Assess for malaria.
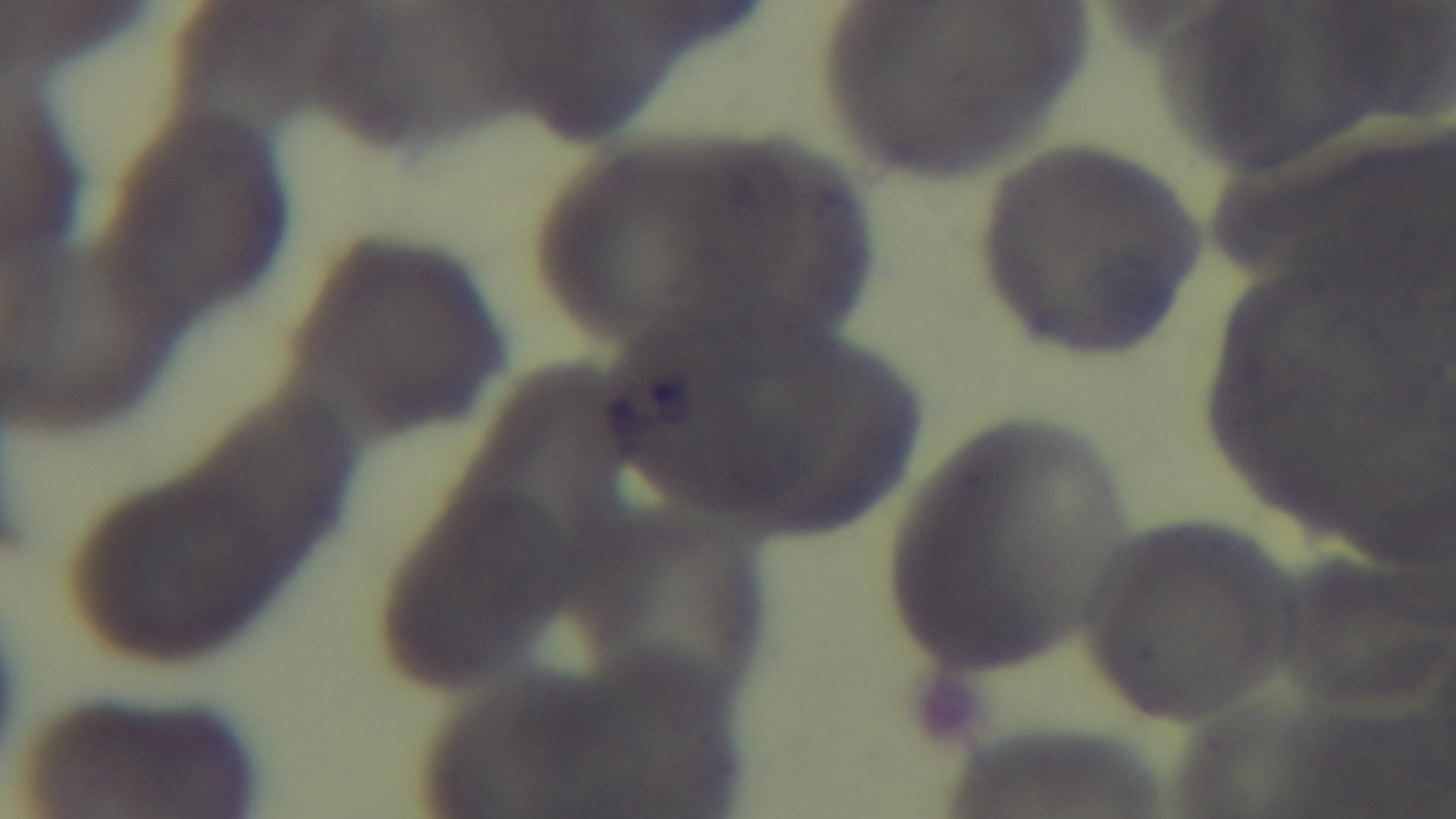
It is uninfected.

modality: light microscopy
stain: Giemsa
capture: mounted 4K digital camera
preparation: thin
field_of_view: single
objective: 100x oil immersion